Outline each Plasmodium vivax-infected red blood cell.
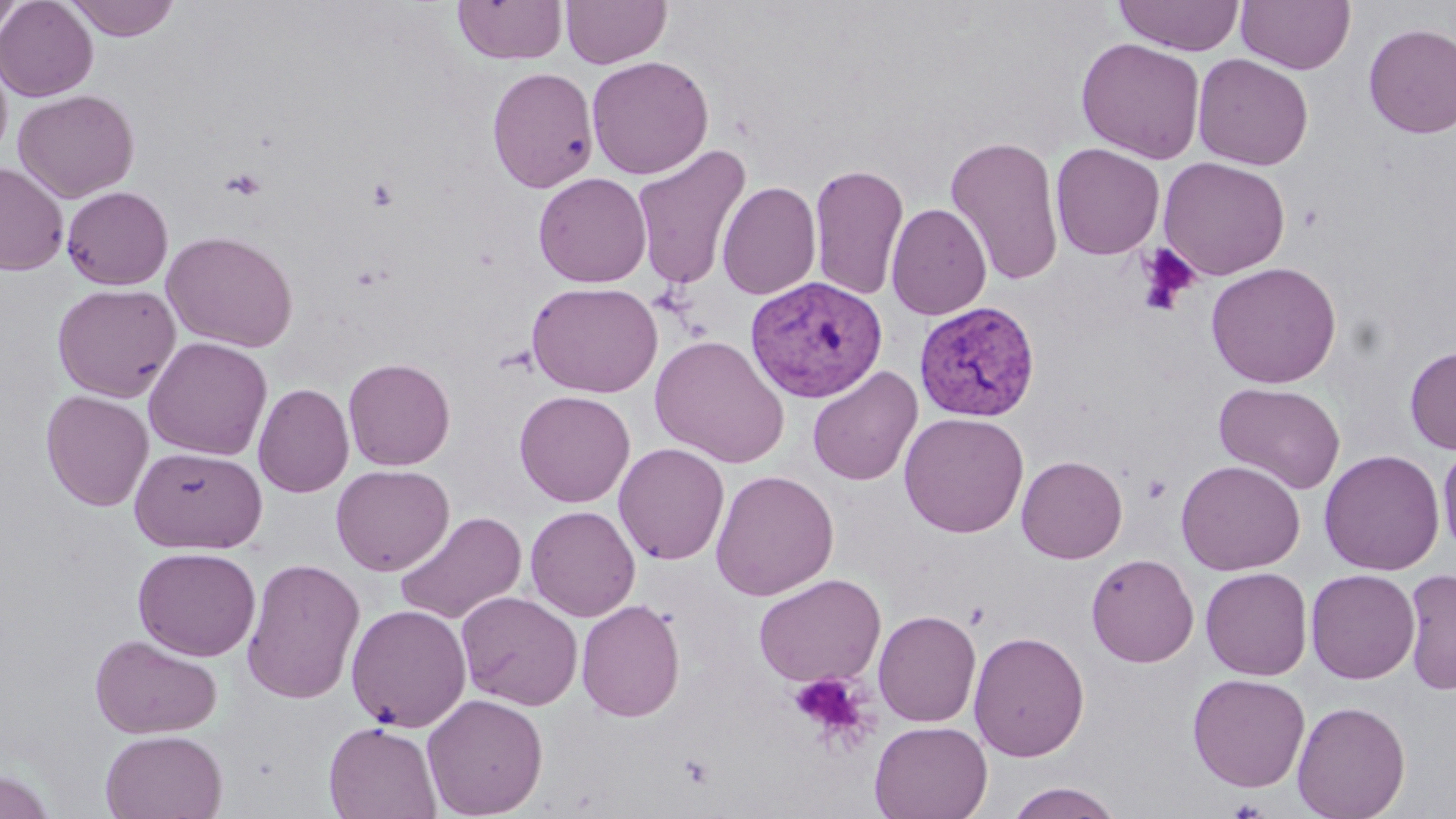

Approximate bounding boxes as named x1/y1/x2/y2 corners in pixels.
Plasmodium vivax-infected red blood cells: (x1=745, y1=276, x2=888, y2=403), (x1=913, y1=300, x2=1041, y2=422).

slide-level diagnosis = Plasmodium vivax
modality = optical microscopy
preparation = thin blood film
platelet locations = approximate bounding boxes as named x1/y1/x2/y2 corners in pixels: (x1=220, y1=168, x2=267, y2=201), (x1=365, y1=177, x2=399, y2=213), (x1=1133, y1=244, x2=1201, y2=316), (x1=1141, y1=473, x2=1172, y2=505), (x1=788, y1=671, x2=874, y2=748)
uninfected red blood cell locations = approximate bounding boxes as named x1/y1/x2/y2 corners in pixels: (x1=0, y1=0, x2=27, y2=38), (x1=0, y1=0, x2=99, y2=101), (x1=64, y1=0, x2=181, y2=41), (x1=561, y1=0, x2=671, y2=68), (x1=1113, y1=0, x2=1246, y2=55), (x1=1236, y1=0, x2=1355, y2=75), (x1=452, y1=1, x2=567, y2=65), (x1=1363, y1=24, x2=1456, y2=139), (x1=1076, y1=37, x2=1206, y2=163), (x1=0, y1=49, x2=13, y2=165), (x1=1192, y1=53, x2=1313, y2=170), (x1=587, y1=55, x2=714, y2=179), (x1=486, y1=66, x2=599, y2=193), (x1=13, y1=89, x2=139, y2=203), (x1=945, y1=135, x2=1065, y2=287), (x1=631, y1=143, x2=753, y2=292), (x1=1049, y1=143, x2=1165, y2=260), (x1=1158, y1=156, x2=1290, y2=280), (x1=0, y1=161, x2=68, y2=275), (x1=808, y1=162, x2=909, y2=301), (x1=533, y1=172, x2=652, y2=287), (x1=716, y1=181, x2=822, y2=300), (x1=61, y1=186, x2=173, y2=290), (x1=886, y1=203, x2=992, y2=320), (x1=161, y1=230, x2=298, y2=353), (x1=1205, y1=261, x2=1342, y2=389), (x1=527, y1=281, x2=663, y2=397), (x1=51, y1=282, x2=181, y2=402), (x1=650, y1=334, x2=790, y2=468), (x1=143, y1=337, x2=273, y2=461), (x1=1404, y1=345, x2=1456, y2=454), (x1=342, y1=358, x2=455, y2=470), (x1=807, y1=366, x2=923, y2=486), (x1=1213, y1=381, x2=1346, y2=494), (x1=253, y1=382, x2=355, y2=498), (x1=40, y1=389, x2=154, y2=511), (x1=514, y1=390, x2=635, y2=507), (x1=899, y1=412, x2=1029, y2=538), (x1=1437, y1=438, x2=1456, y2=560), (x1=613, y1=442, x2=730, y2=565), (x1=130, y1=446, x2=268, y2=554), (x1=1319, y1=449, x2=1444, y2=576), (x1=1016, y1=455, x2=1127, y2=564), (x1=1176, y1=459, x2=1305, y2=576), (x1=331, y1=464, x2=454, y2=576), (x1=711, y1=469, x2=839, y2=601), (x1=525, y1=505, x2=641, y2=622), (x1=394, y1=511, x2=527, y2=626), (x1=132, y1=546, x2=261, y2=661), (x1=1086, y1=553, x2=1199, y2=667), (x1=241, y1=557, x2=366, y2=705), (x1=1200, y1=567, x2=1313, y2=681), (x1=1305, y1=568, x2=1420, y2=684), (x1=1402, y1=569, x2=1456, y2=696), (x1=753, y1=573, x2=886, y2=687), (x1=456, y1=591, x2=583, y2=710), (x1=576, y1=599, x2=686, y2=722), (x1=346, y1=603, x2=472, y2=731), (x1=873, y1=609, x2=981, y2=727), (x1=969, y1=630, x2=1089, y2=762), (x1=90, y1=633, x2=223, y2=739), (x1=1186, y1=673, x2=1310, y2=792), (x1=422, y1=693, x2=549, y2=819), (x1=1292, y1=699, x2=1411, y2=819), (x1=869, y1=720, x2=992, y2=819), (x1=323, y1=721, x2=442, y2=819), (x1=100, y1=729, x2=228, y2=819), (x1=0, y1=768, x2=57, y2=819), (x1=1004, y1=782, x2=1124, y2=818)
field of view = one of a larger specimen
image size = 1456×819 pixels
magnification = 1000x
stain = May-Grünwald-Giemsa